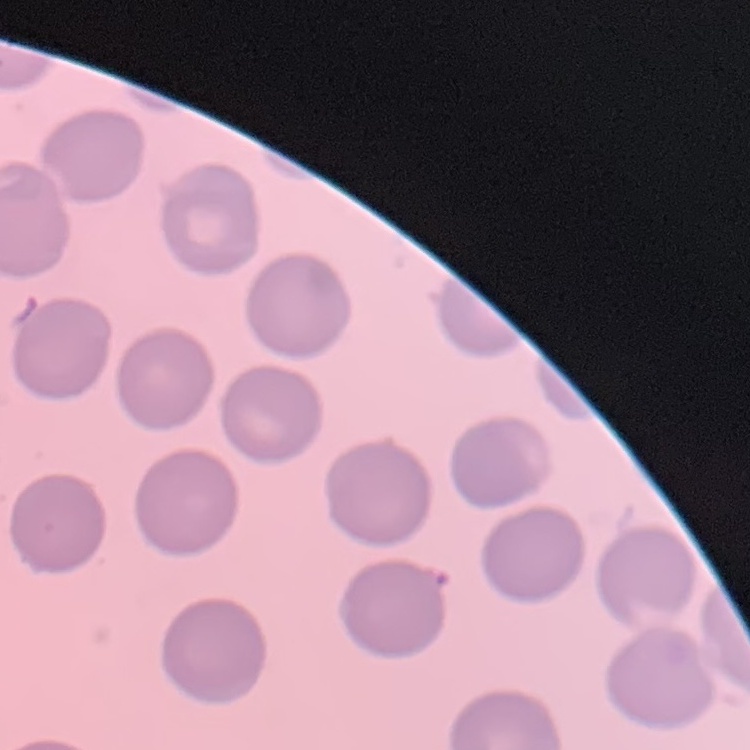

The erythrocytes exhibit no rouleaux formation. Square crop of a larger photomicrograph. Field's or Giemsa stain. Thin peripheral smear.